Assess this cell for malaria.
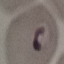

Parasitized.

stain = Giemsa
image type = cell patch, automatically extracted from a larger field of view and resized to 64 × 64 pixels
capture = smartphone camera at the microscope eyepiece
preparation = thin blood film